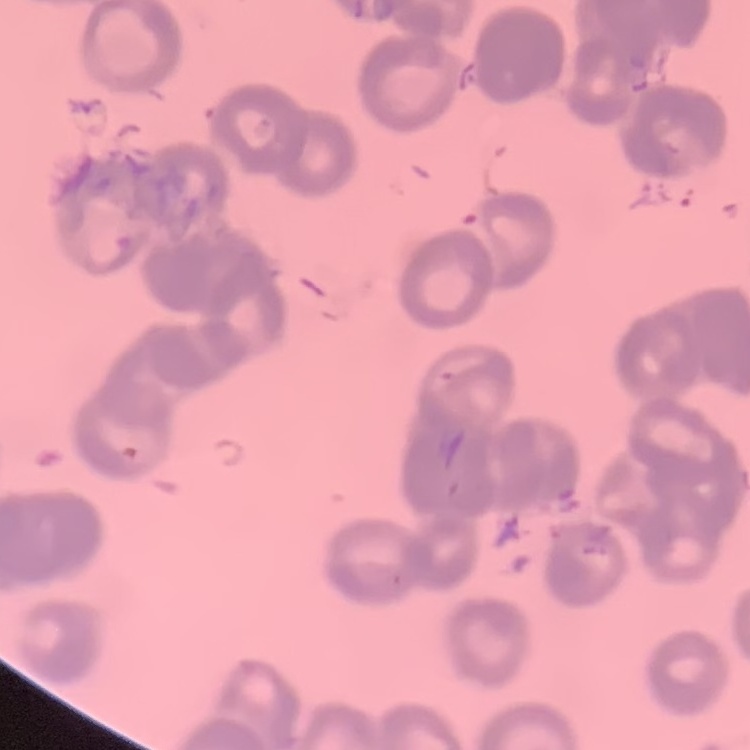

The erythrocytes exhibit rouleaux formation. Thin peripheral smear. Field's or Giemsa stain. Square crop of a larger photomicrograph.